Outline each blood parasite and name the species.
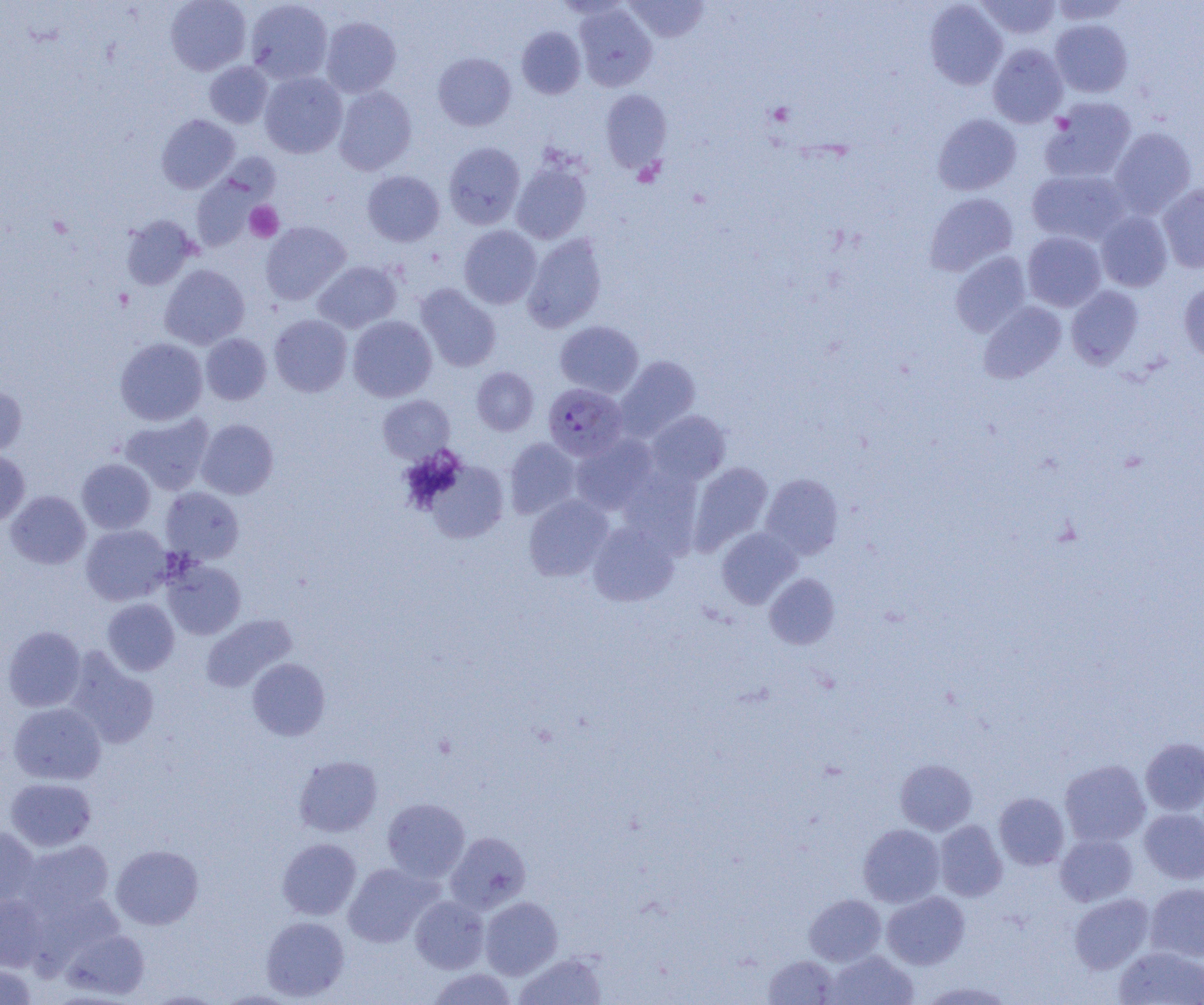
Approximate bounding boxes as [x1, y1, x2, y2] in pixels.
Plasmodium falciparum-infected red blood cells: [543, 383, 628, 461].
No Plasmodium ovale, Plasmodium malariae, Plasmodium vivax, Babesia divergens, or Trypanosoma brucei observed.

Uninfected red blood cell locations: [165, 0, 251, 75], [245, 0, 333, 84], [625, 0, 709, 42], [975, 0, 1061, 40], [924, 1, 1007, 90], [1049, 1, 1130, 25], [574, 4, 657, 91], [320, 16, 401, 97], [1050, 19, 1133, 97], [517, 26, 586, 99], [988, 44, 1068, 127], [433, 52, 516, 130], [205, 61, 273, 128], [259, 72, 347, 158], [334, 86, 417, 175], [600, 89, 672, 173], [1041, 97, 1137, 183], [933, 113, 1021, 195], [157, 114, 239, 193], [1109, 127, 1196, 217], [444, 142, 525, 229], [511, 160, 591, 244], [1027, 169, 1130, 246], [363, 170, 445, 246], [191, 176, 262, 251], [1158, 184, 1204, 272], [925, 193, 1018, 276], [1095, 210, 1173, 291], [121, 215, 198, 290], [261, 221, 351, 305], [459, 225, 542, 309], [1022, 231, 1107, 312], [523, 234, 607, 332], [950, 251, 1031, 337], [312, 261, 402, 333], [159, 264, 250, 350], [1179, 282, 1204, 366], [415, 284, 501, 371], [1066, 285, 1144, 368], [978, 301, 1066, 383], [269, 314, 352, 397], [348, 315, 437, 402], [555, 320, 644, 397], [201, 333, 272, 405], [115, 337, 208, 426], [615, 355, 701, 440], [471, 367, 538, 435], [0, 385, 27, 459], [378, 395, 454, 463], [647, 410, 730, 484], [120, 412, 214, 495], [196, 419, 278, 499], [570, 434, 658, 515], [504, 437, 581, 519], [0, 450, 29, 527], [77, 458, 155, 534], [424, 459, 509, 543], [688, 461, 773, 553], [618, 465, 703, 555], [761, 473, 844, 560], [160, 487, 244, 564], [6, 490, 91, 569], [524, 494, 613, 581], [588, 521, 679, 606], [81, 524, 173, 605], [716, 527, 801, 609], [163, 560, 246, 639], [764, 573, 840, 649], [102, 599, 179, 675], [201, 613, 297, 692], [2, 625, 86, 711], [64, 648, 159, 748], [247, 658, 330, 740], [9, 702, 106, 785], [1140, 737, 1204, 815], [294, 755, 383, 837], [895, 759, 977, 835], [1059, 759, 1151, 846], [5, 778, 96, 850], [994, 792, 1069, 869], [382, 798, 470, 882], [1139, 808, 1204, 884], [934, 820, 1007, 901], [858, 824, 944, 907], [0, 826, 39, 906], [445, 831, 531, 914], [1055, 833, 1138, 906], [278, 838, 361, 920], [17, 840, 114, 918], [111, 844, 203, 929], [343, 863, 439, 947], [1145, 883, 1204, 962], [882, 891, 969, 969], [1069, 893, 1154, 973], [0, 894, 49, 971], [804, 894, 886, 966], [410, 895, 489, 973], [480, 896, 562, 979], [261, 916, 349, 1001], [62, 928, 149, 999], [1114, 946, 1204, 1005], [825, 950, 918, 1005], [514, 952, 607, 1005], [763, 956, 840, 1005], [0, 964, 36, 1004], [428, 968, 517, 1005], [144, 990, 226, 1004], [216, 990, 301, 1004]. Platelet locations: [245, 201, 283, 242]. Slide-level diagnosis: Plasmodium falciparum. One field of a larger specimen. Light microscopy. Captured at 1000x magnification. Thin blood film. Image is 1204×1005 pixels.